Locate and identify every blood parasite.
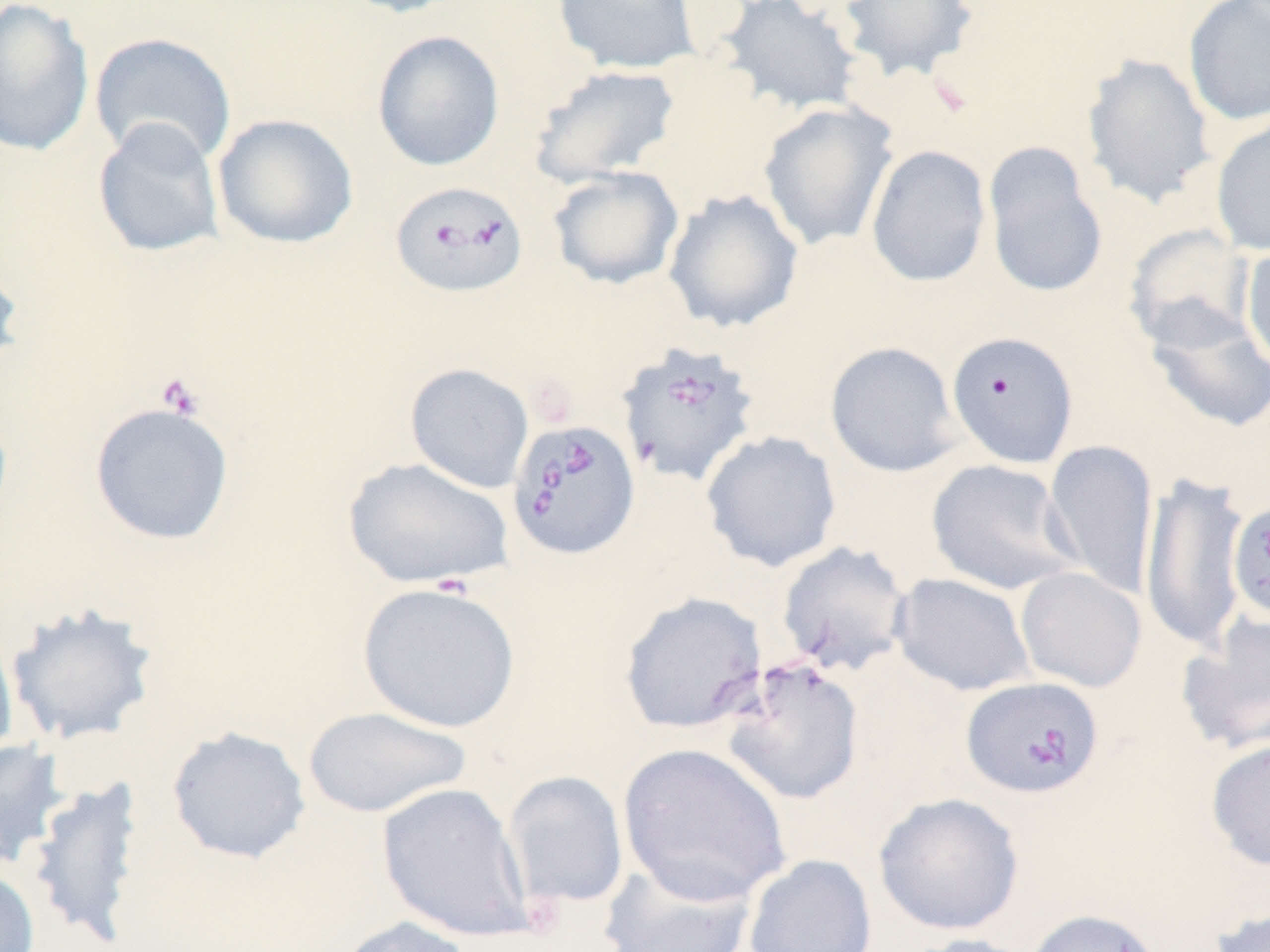
Approximate bounding boxes as named x1/y1/x2/y2 corners in pixels.
Babesia divergens-infected red blood cells: (x1=389, y1=180, x2=530, y2=299), (x1=616, y1=340, x2=762, y2=489), (x1=506, y1=417, x2=641, y2=561), (x1=961, y1=676, x2=1104, y2=799).
No Plasmodium falciparum, Plasmodium ovale, Plasmodium malariae, Plasmodium vivax, or Trypanosoma brucei observed.

Uninfected red blood cell locations: (x1=0, y1=0, x2=95, y2=158), (x1=333, y1=0, x2=464, y2=19), (x1=551, y1=0, x2=701, y2=75), (x1=715, y1=0, x2=865, y2=117), (x1=835, y1=0, x2=981, y2=84), (x1=1183, y1=1, x2=1270, y2=126), (x1=371, y1=29, x2=505, y2=171), (x1=89, y1=31, x2=237, y2=168), (x1=1080, y1=52, x2=1218, y2=210), (x1=527, y1=64, x2=682, y2=187), (x1=758, y1=102, x2=900, y2=251), (x1=212, y1=113, x2=359, y2=249), (x1=1210, y1=114, x2=1270, y2=256), (x1=91, y1=117, x2=226, y2=257), (x1=981, y1=142, x2=1109, y2=300), (x1=866, y1=144, x2=992, y2=288), (x1=547, y1=166, x2=684, y2=290), (x1=663, y1=188, x2=805, y2=334), (x1=1123, y1=224, x2=1256, y2=352), (x1=1240, y1=244, x2=1270, y2=375), (x1=0, y1=252, x2=26, y2=384), (x1=1142, y1=303, x2=1270, y2=433), (x1=946, y1=330, x2=1079, y2=468), (x1=825, y1=341, x2=963, y2=477), (x1=404, y1=362, x2=535, y2=493), (x1=89, y1=401, x2=235, y2=545), (x1=700, y1=430, x2=843, y2=572), (x1=1043, y1=438, x2=1160, y2=599), (x1=342, y1=456, x2=514, y2=589), (x1=926, y1=458, x2=1080, y2=596), (x1=1140, y1=470, x2=1249, y2=654), (x1=1227, y1=500, x2=1270, y2=622), (x1=775, y1=541, x2=914, y2=677), (x1=1015, y1=566, x2=1147, y2=693), (x1=890, y1=573, x2=1036, y2=696), (x1=357, y1=581, x2=521, y2=733), (x1=618, y1=591, x2=768, y2=734), (x1=5, y1=603, x2=159, y2=747), (x1=1176, y1=614, x2=1270, y2=756), (x1=0, y1=623, x2=19, y2=763), (x1=719, y1=657, x2=866, y2=806), (x1=302, y1=705, x2=472, y2=819), (x1=166, y1=725, x2=312, y2=864), (x1=1204, y1=737, x2=1270, y2=871), (x1=0, y1=739, x2=70, y2=870), (x1=616, y1=740, x2=791, y2=906), (x1=502, y1=770, x2=629, y2=911), (x1=25, y1=776, x2=147, y2=948), (x1=376, y1=782, x2=533, y2=941), (x1=873, y1=792, x2=1025, y2=935), (x1=742, y1=854, x2=877, y2=952), (x1=598, y1=859, x2=758, y2=952), (x1=0, y1=866, x2=41, y2=952), (x1=1023, y1=907, x2=1163, y2=952), (x1=1206, y1=908, x2=1270, y2=952), (x1=329, y1=915, x2=477, y2=952), (x1=909, y1=933, x2=1038, y2=952). Platelet locations: (x1=154, y1=372, x2=205, y2=419). Slide-level diagnosis: Babesia divergens. Light microscopy. Image is 1270×952 pixels. Captured at 1000x magnification. May-Grünwald-Giemsa stain. Single field of view. Thin blood film.